Classify this cell by malaria status.
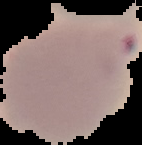
It is parasitized.

Summary:
  - Image type: segmented cell region with the area outside set to black
  - Preparation: thin blood smear
  - Image size: 142×145 pixels